Name the parasite shown.
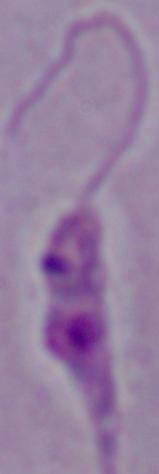

This is Leishmania.

Summary:
  - Magnification: 1000x
  - Modality: micrograph